Give the preparation type.
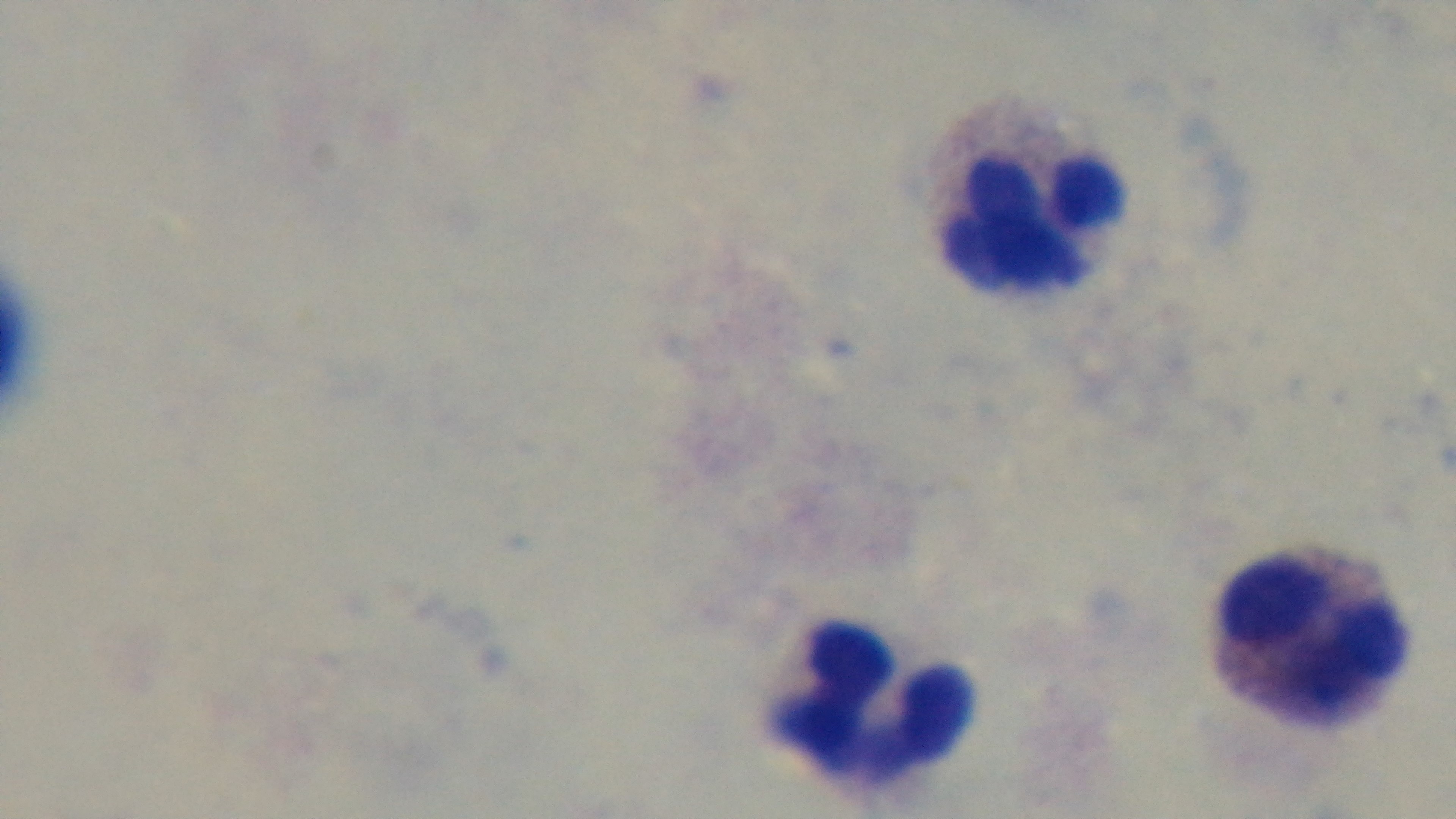
A thick smear.

Giemsa stain. Malaria status: uninfected. Photomicrograph. Mounted 4K digital camera. 100x oil-immersion objective. One field from the slide.